Locate every blood parasite and identify its species.
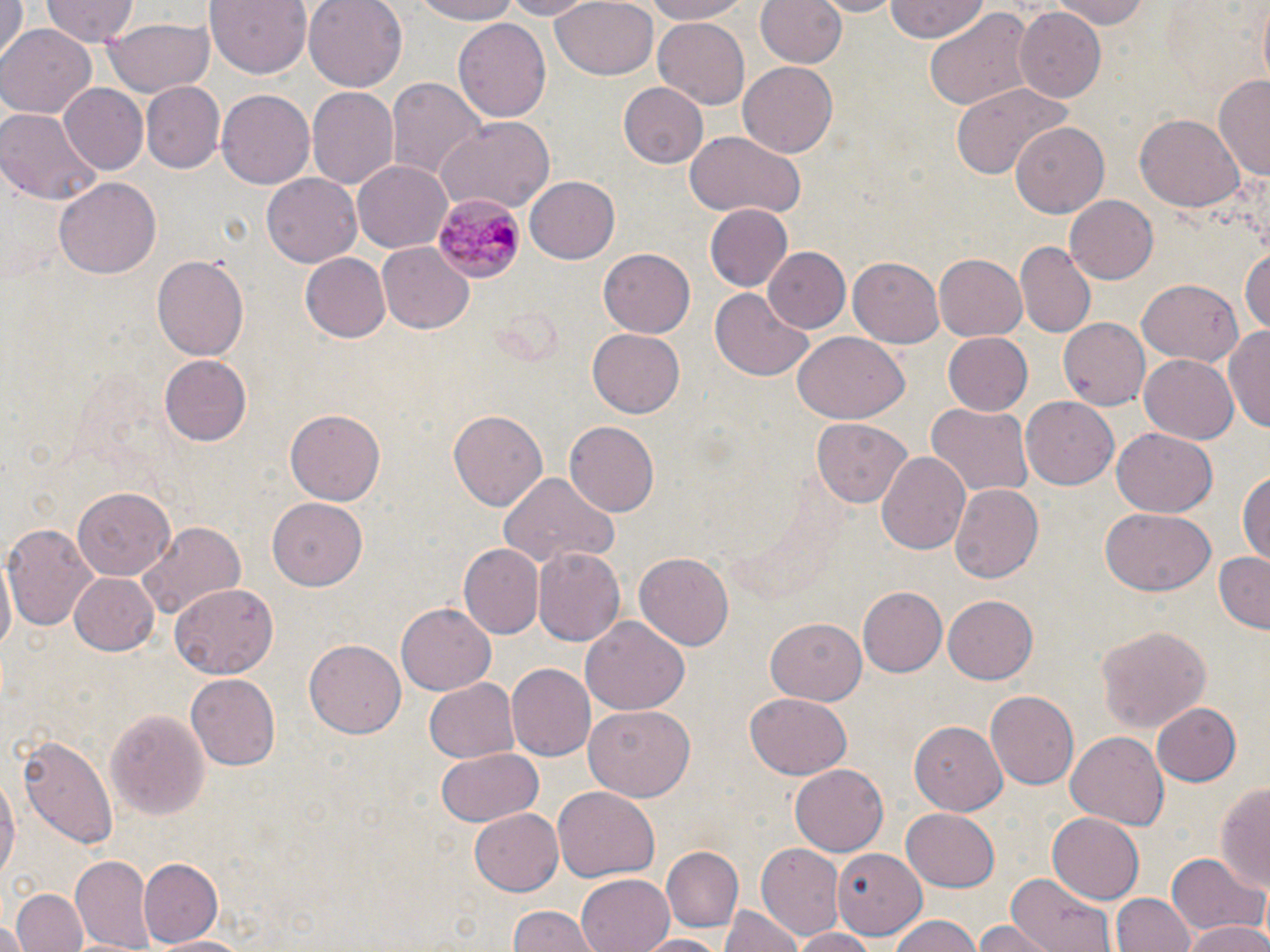

Approximate bounding boxes as named x1/y1/x2/y2 corners in pixels.
Plasmodium malariae-infected red blood cells: (x1=434, y1=195, x2=522, y2=280).
No Plasmodium falciparum, Plasmodium ovale, Plasmodium vivax, Babesia divergens, or Trypanosoma brucei observed.

Uninfected red blood cell locations: (x1=41, y1=0, x2=140, y2=46), (x1=206, y1=0, x2=312, y2=77), (x1=304, y1=0, x2=407, y2=92), (x1=410, y1=0, x2=528, y2=25), (x1=492, y1=0, x2=604, y2=20), (x1=550, y1=0, x2=658, y2=81), (x1=640, y1=0, x2=753, y2=25), (x1=756, y1=0, x2=847, y2=70), (x1=809, y1=0, x2=904, y2=16), (x1=883, y1=0, x2=991, y2=47), (x1=1055, y1=0, x2=1152, y2=28), (x1=0, y1=1, x2=23, y2=67), (x1=1253, y1=2, x2=1270, y2=90), (x1=924, y1=7, x2=1036, y2=116), (x1=1014, y1=9, x2=1104, y2=101), (x1=103, y1=17, x2=214, y2=99), (x1=455, y1=17, x2=552, y2=121), (x1=654, y1=18, x2=751, y2=108), (x1=0, y1=24, x2=94, y2=119), (x1=737, y1=59, x2=837, y2=154), (x1=388, y1=75, x2=486, y2=179), (x1=1215, y1=76, x2=1270, y2=180), (x1=140, y1=81, x2=224, y2=173), (x1=618, y1=81, x2=709, y2=168), (x1=952, y1=82, x2=1067, y2=182), (x1=58, y1=83, x2=147, y2=173), (x1=307, y1=87, x2=399, y2=192), (x1=216, y1=91, x2=313, y2=189), (x1=0, y1=108, x2=103, y2=205), (x1=1136, y1=112, x2=1243, y2=212), (x1=435, y1=116, x2=555, y2=211), (x1=1011, y1=124, x2=1108, y2=218), (x1=684, y1=132, x2=805, y2=218), (x1=352, y1=159, x2=452, y2=250), (x1=262, y1=173, x2=362, y2=268), (x1=524, y1=175, x2=620, y2=264), (x1=54, y1=176, x2=161, y2=279), (x1=1066, y1=196, x2=1158, y2=282), (x1=706, y1=204, x2=794, y2=292), (x1=1016, y1=243, x2=1095, y2=338), (x1=378, y1=245, x2=473, y2=334), (x1=763, y1=246, x2=850, y2=332), (x1=1241, y1=246, x2=1270, y2=339), (x1=599, y1=247, x2=696, y2=337), (x1=298, y1=253, x2=390, y2=342), (x1=848, y1=253, x2=944, y2=346), (x1=933, y1=254, x2=1027, y2=343), (x1=152, y1=255, x2=248, y2=363), (x1=1138, y1=280, x2=1244, y2=366), (x1=711, y1=290, x2=813, y2=379), (x1=1058, y1=317, x2=1150, y2=411), (x1=1226, y1=324, x2=1270, y2=437), (x1=587, y1=327, x2=685, y2=418), (x1=791, y1=332, x2=907, y2=424), (x1=942, y1=332, x2=1033, y2=416), (x1=1138, y1=352, x2=1239, y2=443), (x1=159, y1=354, x2=252, y2=447), (x1=1021, y1=393, x2=1119, y2=486), (x1=924, y1=403, x2=1033, y2=501), (x1=449, y1=409, x2=548, y2=511), (x1=286, y1=410, x2=385, y2=503), (x1=812, y1=418, x2=912, y2=507), (x1=564, y1=422, x2=658, y2=516), (x1=1111, y1=428, x2=1217, y2=517), (x1=876, y1=451, x2=972, y2=558), (x1=1238, y1=469, x2=1270, y2=566), (x1=497, y1=474, x2=616, y2=567), (x1=948, y1=484, x2=1041, y2=585), (x1=70, y1=487, x2=173, y2=578), (x1=268, y1=497, x2=367, y2=590), (x1=1100, y1=508, x2=1214, y2=595), (x1=135, y1=520, x2=245, y2=621), (x1=3, y1=521, x2=100, y2=630), (x1=457, y1=543, x2=543, y2=639), (x1=532, y1=548, x2=625, y2=648), (x1=1213, y1=552, x2=1270, y2=633), (x1=0, y1=553, x2=16, y2=664), (x1=634, y1=553, x2=736, y2=649), (x1=71, y1=572, x2=160, y2=656), (x1=170, y1=584, x2=276, y2=678), (x1=857, y1=587, x2=945, y2=678), (x1=943, y1=594, x2=1039, y2=684), (x1=397, y1=603, x2=495, y2=693), (x1=580, y1=614, x2=690, y2=717), (x1=766, y1=618, x2=868, y2=704), (x1=1094, y1=622, x2=1212, y2=736), (x1=304, y1=637, x2=407, y2=738), (x1=505, y1=663, x2=594, y2=761), (x1=185, y1=675, x2=278, y2=770), (x1=423, y1=679, x2=518, y2=761), (x1=987, y1=687, x2=1080, y2=789), (x1=744, y1=692, x2=852, y2=779), (x1=1153, y1=701, x2=1242, y2=786), (x1=584, y1=704, x2=696, y2=801), (x1=106, y1=707, x2=211, y2=821), (x1=910, y1=720, x2=1006, y2=813), (x1=1065, y1=729, x2=1169, y2=828), (x1=16, y1=734, x2=118, y2=852), (x1=435, y1=745, x2=543, y2=829), (x1=790, y1=764, x2=888, y2=854), (x1=0, y1=774, x2=18, y2=889), (x1=1215, y1=778, x2=1270, y2=894), (x1=554, y1=786, x2=659, y2=882), (x1=467, y1=807, x2=562, y2=896), (x1=900, y1=809, x2=999, y2=891), (x1=1046, y1=812, x2=1146, y2=903), (x1=756, y1=845, x2=844, y2=942), (x1=662, y1=846, x2=744, y2=931), (x1=831, y1=849, x2=928, y2=937), (x1=1169, y1=853, x2=1263, y2=939), (x1=70, y1=856, x2=154, y2=949), (x1=138, y1=857, x2=224, y2=949), (x1=577, y1=874, x2=676, y2=952), (x1=1006, y1=875, x2=1119, y2=952), (x1=12, y1=888, x2=87, y2=952), (x1=1111, y1=892, x2=1194, y2=952), (x1=722, y1=905, x2=800, y2=952), (x1=506, y1=907, x2=598, y2=952), (x1=886, y1=914, x2=984, y2=952), (x1=0, y1=919, x2=26, y2=952), (x1=976, y1=921, x2=1053, y2=952), (x1=1183, y1=923, x2=1270, y2=952), (x1=788, y1=927, x2=881, y2=952), (x1=153, y1=933, x2=253, y2=952), (x1=638, y1=933, x2=726, y2=952). Slide-level diagnosis: Plasmodium malariae. Captured at 1000x magnification. Image is 1270×952 pixels. Thin blood smear. Single field of view. May-Grünwald-Giemsa-stained preparation. Light microscopy.